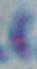
Toxoplasma gondii is shown. Micrograph. Captured at 1000x magnification.